Locate every Plasmodium falciparum-infected red blood cell.
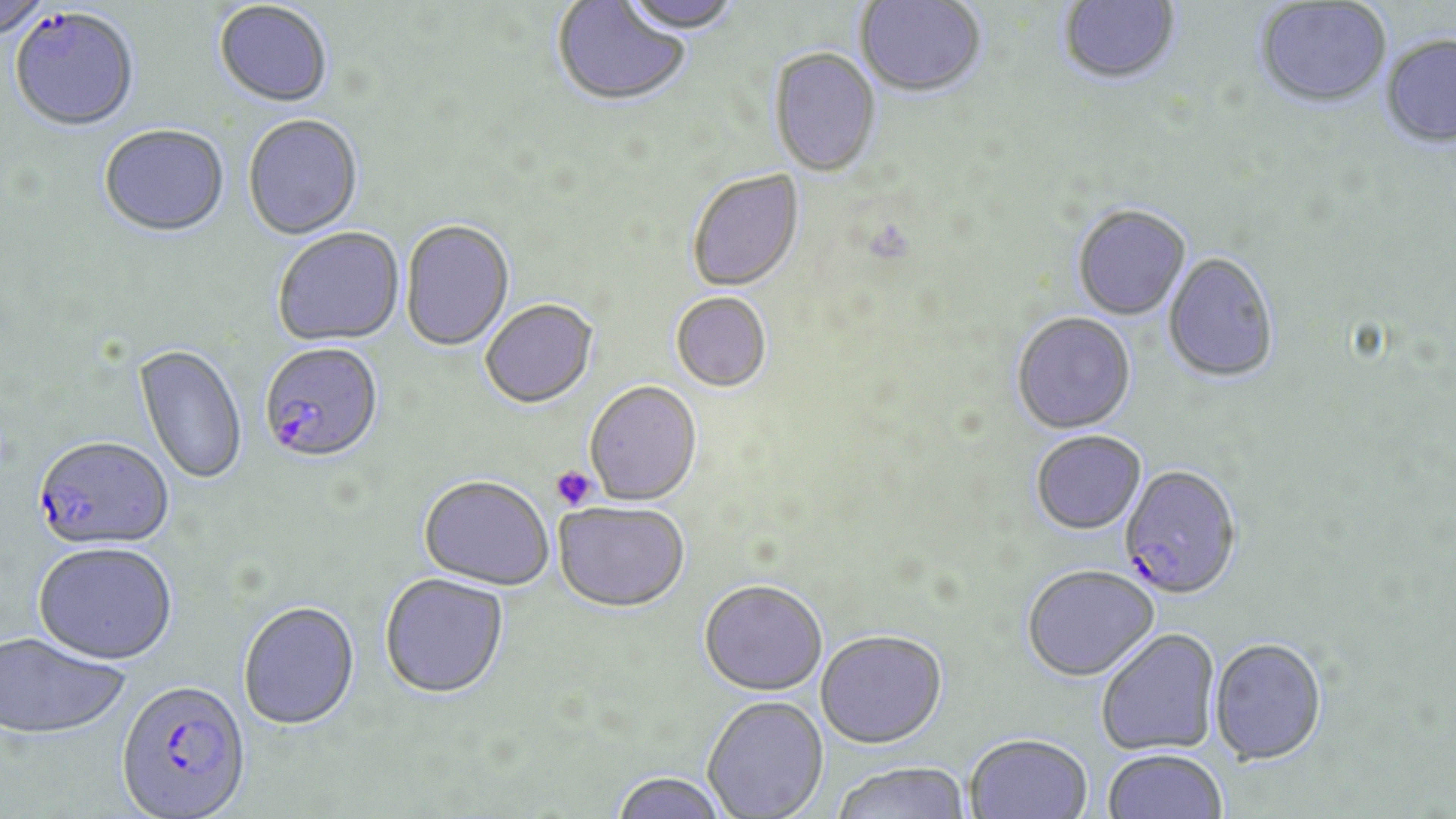
Approximate bounding boxes as (x1,y1)-(x2,y2) corner pairs in pixels.
Plasmodium falciparum-infected red blood cells: (8,10)-(140,133), (259,344)-(384,467), (33,439)-(173,553), (1120,467)-(1243,602), (115,682)-(252,819).

Platelet locations: (550,465)-(599,511). Uninfected red blood cell locations: (0,0)-(54,43), (619,0)-(741,37), (855,0)-(987,100), (1058,0)-(1181,88), (552,1)-(690,109), (1255,2)-(1391,111), (213,3)-(333,110), (1380,37)-(1456,149), (769,49)-(882,179), (243,116)-(363,241), (98,126)-(230,240), (687,170)-(805,293), (1072,206)-(1191,321), (401,221)-(515,353), (273,229)-(406,348), (1162,254)-(1280,385), (671,293)-(772,394), (481,300)-(599,411), (1012,314)-(1136,435), (132,345)-(248,486), (585,382)-(702,507), (1031,432)-(1147,536), (417,478)-(554,592), (553,503)-(690,614), (33,545)-(178,668), (1021,565)-(1159,683), (379,575)-(509,701), (699,578)-(828,695), (238,603)-(360,733), (1096,628)-(1221,756), (815,630)-(947,748), (1,633)-(130,742), (1209,638)-(1328,765), (702,695)-(828,819), (964,733)-(1092,819), (1102,748)-(1227,819), (832,760)-(971,819), (610,771)-(730,819). Slide-level diagnosis: Plasmodium falciparum. Light microscopy. 1000x magnification. Image is 1456×819 pixels. May-Grünwald-Giemsa-stained preparation. Thin blood film. Single field of view.